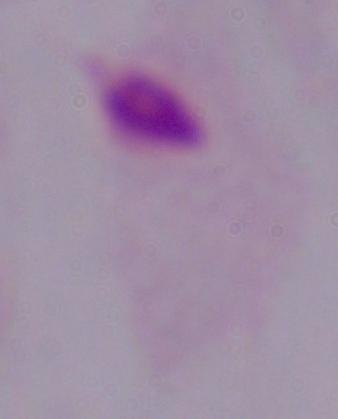
Summary:
  - Modality: photomicrograph
  - Identification: trichomonad
  - Magnification: 1000x